Report the malaria status of this cell.
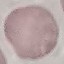

It is uninfected.

Cell patch, automatically extracted from a larger field of view and resized to 64 × 64 pixels. Photographed with a smartphone camera at the microscope eyepiece. Thin blood film. Giemsa-stained preparation.